Name the parasite shown.
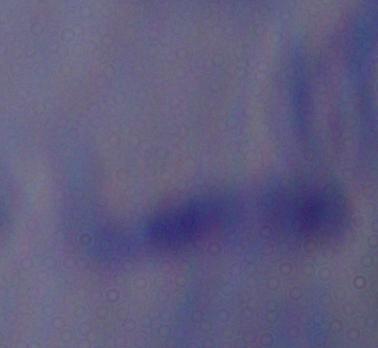

A trypanosome.

Summary:
  - Magnification: 1000x
  - Modality: micrograph